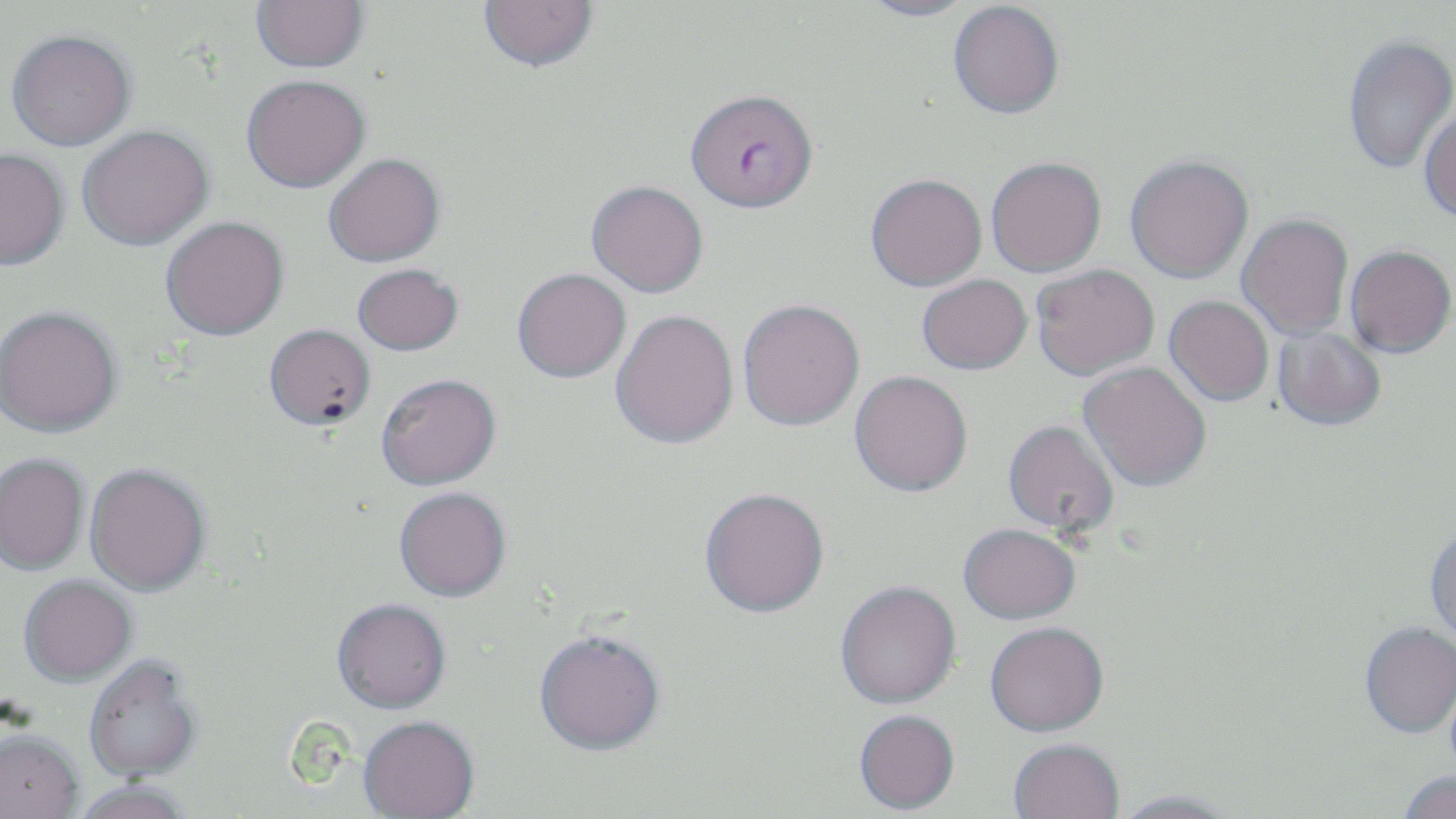
Summary:
  - Coordinate format: approximate bounding boxes as (x1,y1)-(x2,y2) corner pairs in pixels
  - Uninfected red blood cell locations: (251,0)-(369,72), (479,0)-(598,71), (857,1)-(978,21), (949,1)-(1064,118), (6,29)-(135,151), (1343,34)-(1455,174), (241,74)-(370,192), (1419,105)-(1456,223), (77,124)-(213,250), (0,148)-(70,270), (323,153)-(444,266), (1125,155)-(1253,283), (986,156)-(1106,277), (866,173)-(987,290), (586,180)-(708,298), (1237,213)-(1353,341), (161,215)-(289,340), (1345,245)-(1455,358), (352,263)-(463,356), (1031,264)-(1159,380), (512,268)-(630,382), (917,274)-(1032,375), (1164,295)-(1274,407), (737,298)-(864,431), (0,305)-(122,437), (610,310)-(739,450), (264,324)-(376,430), (1272,327)-(1386,432), (1079,363)-(1211,494), (849,371)-(972,499), (376,373)-(501,490), (1002,421)-(1120,540), (0,453)-(90,575), (84,463)-(211,596), (394,488)-(511,603), (700,492)-(829,622), (1425,525)-(1456,647), (958,526)-(1080,628), (19,576)-(137,687), (836,584)-(961,711), (332,600)-(452,716), (1360,624)-(1456,740), (985,625)-(1109,740), (533,634)-(665,760), (84,658)-(202,785), (854,713)-(960,816), (358,719)-(480,819), (0,733)-(84,819), (1008,742)-(1124,819), (1397,772)-(1456,819), (72,783)-(194,819), (1111,792)-(1240,819)
  - Plasmodium falciparum-infected red blood cell locations: (686,88)-(818,211)
  - Slide-level diagnosis: Plasmodium falciparum
  - Image size: 1456×819 pixels
  - Preparation: thin blood film
  - Magnification: 1000x
  - Modality: light microscopy
  - Field of view: single
  - Stain: May-Grünwald-Giemsa